State which parasite is depicted.
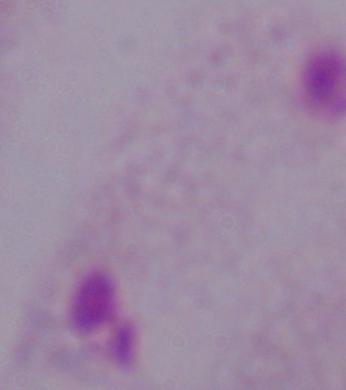
A trichomonad.

Summary:
  - Modality: micrograph
  - Magnification: 1000x